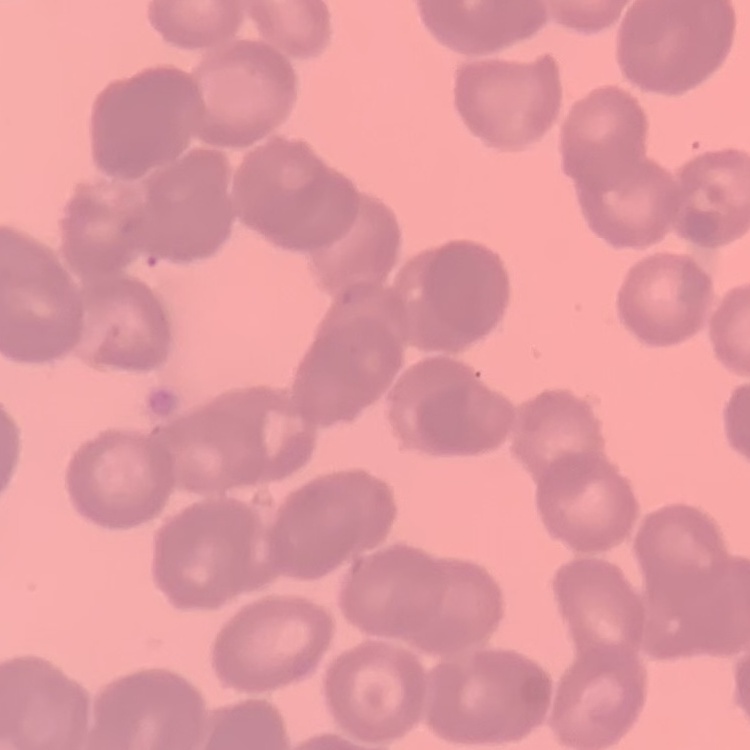
red_blood_cell_morphology: rouleaux formation
image_type: one tile cut from a larger photomicrograph
preparation: thin blood smear
stain: Field's or Giemsa